State the blood parasite species.
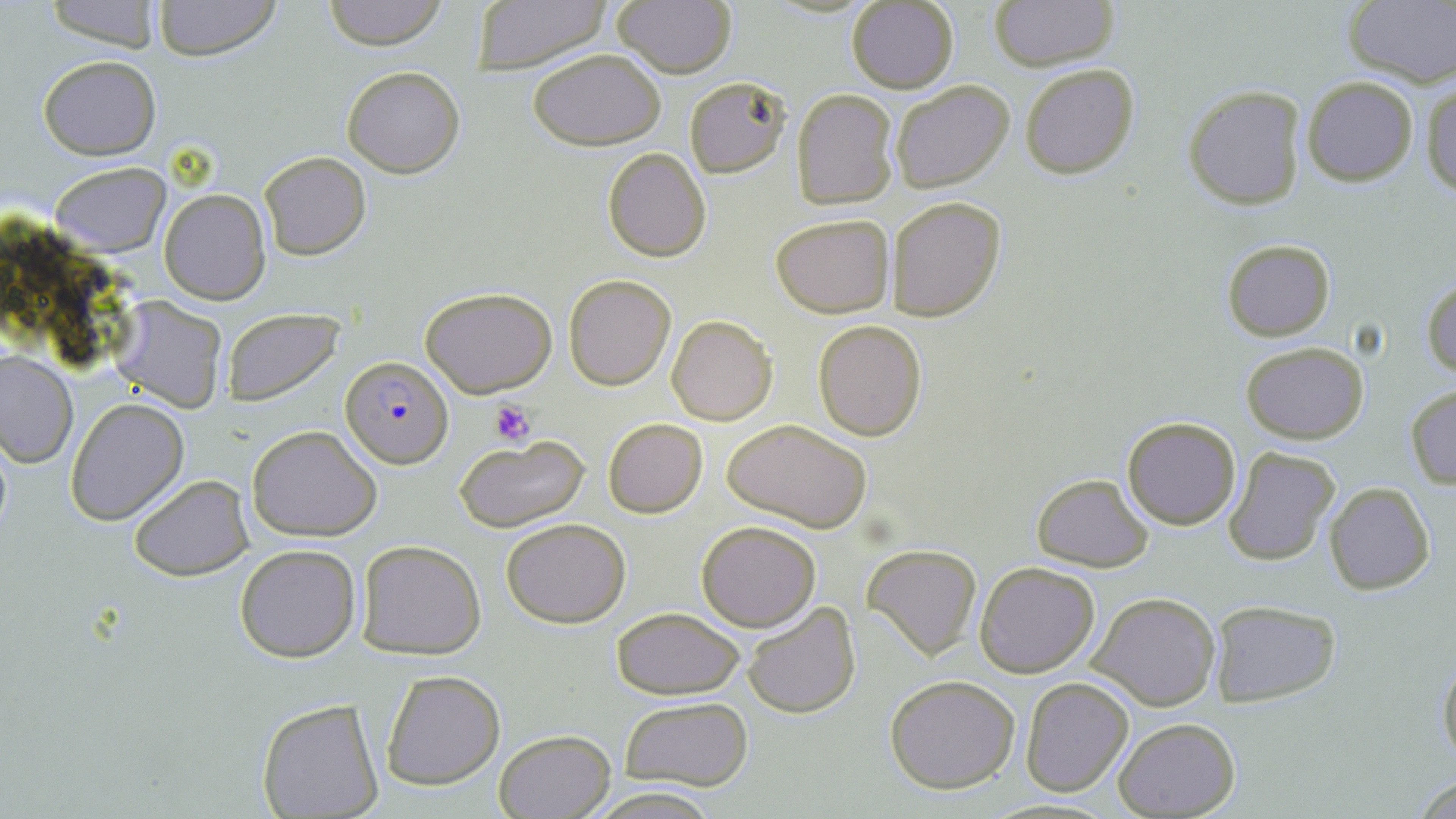
Plasmodium falciparum.

{
  "platelet_locations": "approximate bounding boxes as (x1, y1, x2, y2) in pixels: (490, 400, 534, 447)",
  "plasmodium_falciparum_infected_red_blood_cell_locations": "approximate bounding boxes as (x1, y1, x2, y2) in pixels: (341, 358, 454, 467)",
  "magnification": "1000x",
  "stain": "May-Grünwald-Giemsa",
  "uninfected_red_blood_cell_locations": "approximate bounding boxes as (x1, y1, x2, y2) in pixels: (150, 0, 283, 62), (321, 0, 449, 50), (467, 0, 613, 73), (988, 0, 1122, 72), (43, 1, 161, 50), (846, 1, 960, 94), (612, 2, 738, 79), (1342, 2, 1456, 85), (529, 48, 666, 152), (37, 54, 160, 159), (1020, 63, 1141, 180), (342, 64, 465, 179), (684, 75, 793, 178), (1299, 75, 1418, 187), (889, 78, 1015, 194), (1423, 82, 1456, 200), (1183, 84, 1307, 209), (791, 90, 899, 209), (603, 148, 712, 262), (258, 150, 370, 260), (51, 161, 170, 257), (159, 190, 271, 305), (886, 196, 1006, 321), (771, 215, 894, 316), (1222, 239, 1334, 341), (564, 275, 677, 390), (1423, 279, 1456, 379), (419, 285, 557, 398), (112, 297, 227, 412), (223, 309, 342, 405), (666, 314, 777, 425), (812, 319, 927, 441), (1241, 342, 1369, 443), (0, 348, 78, 467), (1405, 384, 1456, 488), (66, 400, 189, 526), (720, 417, 873, 530), (1122, 417, 1240, 530), (603, 418, 707, 517), (246, 425, 382, 541), (454, 435, 590, 532), (1222, 446, 1341, 566), (1030, 471, 1154, 572), (128, 473, 254, 582), (1324, 481, 1435, 595), (501, 517, 631, 629), (697, 521, 822, 631), (355, 539, 487, 659), (234, 543, 362, 663), (862, 544, 982, 660), (974, 562, 1101, 679), (1089, 591, 1222, 711), (1208, 600, 1342, 707), (742, 601, 860, 720), (608, 606, 747, 699), (1437, 649, 1456, 771), (381, 671, 505, 789), (884, 675, 1020, 791), (1021, 677, 1134, 796), (618, 696, 754, 790), (253, 697, 385, 818), (1112, 717, 1239, 818), (492, 727, 618, 819), (1407, 772, 1456, 819), (582, 785, 723, 819)",
  "image_size": "1456×819 pixels",
  "preparation": "thin blood film",
  "modality": "optical microscopy",
  "field_of_view": "single"
}